Name the blood parasite species.
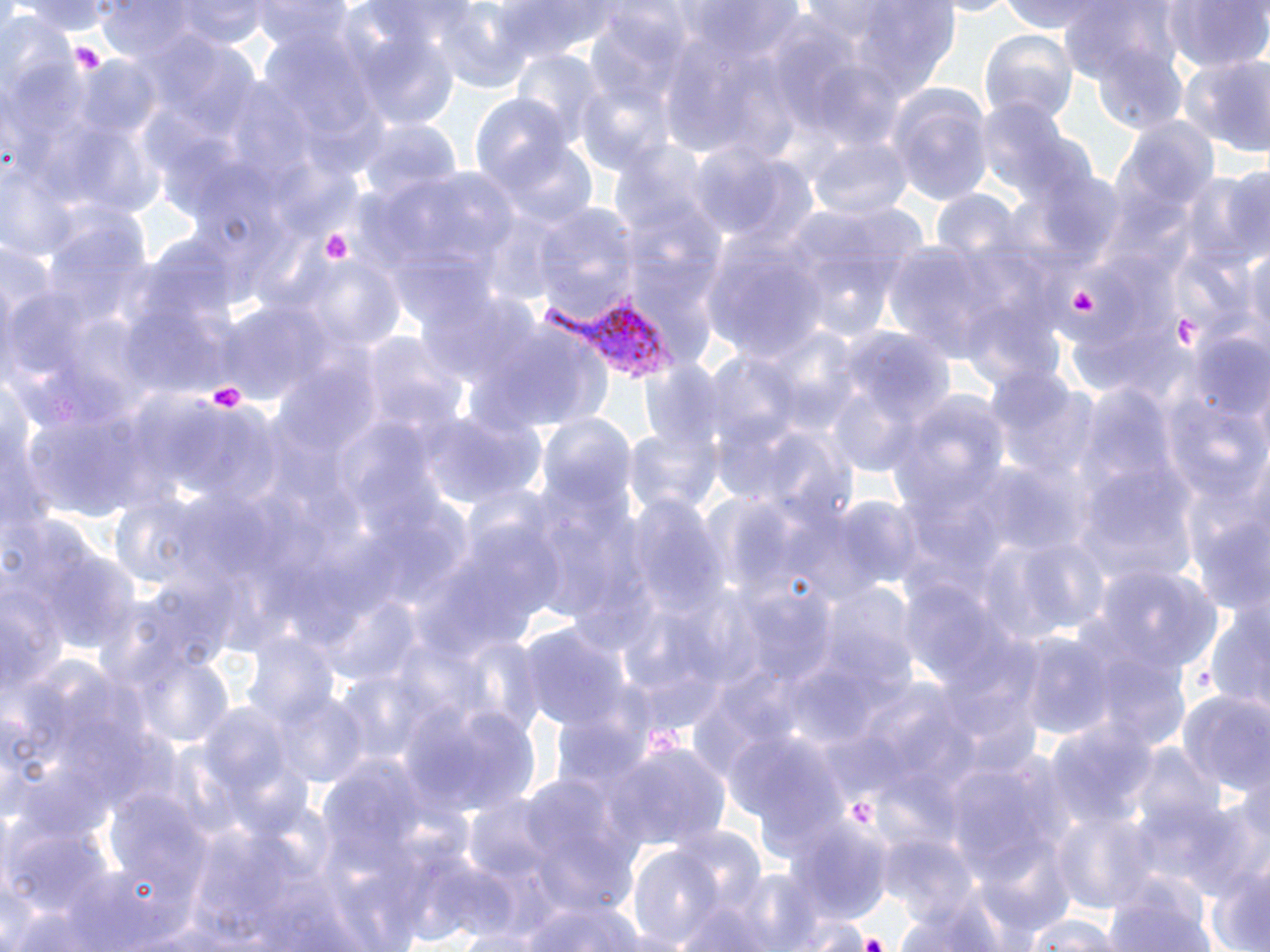
Plasmodium vivax.

Approximate bounding boxes as named x1/y1/x2/y2 corners in pixels. Plasmodium vivax-infected red blood cell locations: (x1=541, y1=294, x2=683, y2=387). Platelet locations: (x1=65, y1=41, x2=103, y2=73), (x1=319, y1=227, x2=355, y2=266), (x1=1070, y1=285, x2=1100, y2=315), (x1=1173, y1=315, x2=1200, y2=348), (x1=205, y1=380, x2=250, y2=417), (x1=850, y1=796, x2=877, y2=824), (x1=856, y1=931, x2=888, y2=950). Uninfected red blood cell locations: (x1=14, y1=0, x2=119, y2=35), (x1=251, y1=0, x2=357, y2=53), (x1=993, y1=0, x2=1128, y2=34), (x1=1161, y1=0, x2=1270, y2=76), (x1=176, y1=1, x2=270, y2=47), (x1=499, y1=1, x2=626, y2=59), (x1=831, y1=2, x2=963, y2=98), (x1=1056, y1=2, x2=1181, y2=78), (x1=98, y1=3, x2=198, y2=60), (x1=425, y1=5, x2=539, y2=91), (x1=0, y1=16, x2=81, y2=103), (x1=351, y1=22, x2=463, y2=130), (x1=978, y1=31, x2=1078, y2=122), (x1=1090, y1=41, x2=1190, y2=135), (x1=512, y1=49, x2=609, y2=147), (x1=1182, y1=53, x2=1270, y2=160), (x1=75, y1=61, x2=165, y2=146), (x1=575, y1=86, x2=675, y2=178), (x1=888, y1=86, x2=991, y2=204), (x1=469, y1=92, x2=575, y2=203), (x1=976, y1=98, x2=1077, y2=205), (x1=1119, y1=117, x2=1219, y2=219), (x1=358, y1=119, x2=461, y2=208), (x1=807, y1=136, x2=912, y2=223), (x1=496, y1=139, x2=599, y2=229), (x1=1185, y1=169, x2=1270, y2=267), (x1=930, y1=191, x2=1023, y2=272), (x1=620, y1=197, x2=727, y2=338), (x1=531, y1=206, x2=642, y2=324), (x1=701, y1=229, x2=832, y2=364), (x1=1241, y1=242, x2=1270, y2=365), (x1=289, y1=254, x2=403, y2=360), (x1=418, y1=285, x2=535, y2=386), (x1=219, y1=300, x2=336, y2=407), (x1=470, y1=317, x2=610, y2=435), (x1=357, y1=329, x2=468, y2=440), (x1=1192, y1=335, x2=1270, y2=424), (x1=1, y1=381, x2=48, y2=544), (x1=888, y1=392, x2=1010, y2=520), (x1=422, y1=411, x2=545, y2=513), (x1=624, y1=422, x2=724, y2=522), (x1=1075, y1=477, x2=1199, y2=591), (x1=618, y1=494, x2=725, y2=624), (x1=995, y1=533, x2=1111, y2=644), (x1=1094, y1=568, x2=1222, y2=673), (x1=0, y1=582, x2=61, y2=705), (x1=1203, y1=607, x2=1270, y2=712), (x1=516, y1=622, x2=635, y2=738), (x1=1008, y1=627, x2=1116, y2=739), (x1=244, y1=633, x2=342, y2=730), (x1=127, y1=647, x2=237, y2=749), (x1=1083, y1=650, x2=1191, y2=755), (x1=269, y1=691, x2=369, y2=786), (x1=1181, y1=691, x2=1270, y2=795), (x1=408, y1=699, x2=541, y2=820), (x1=198, y1=705, x2=296, y2=808), (x1=1051, y1=724, x2=1158, y2=827), (x1=604, y1=739, x2=729, y2=857), (x1=1135, y1=744, x2=1224, y2=832), (x1=939, y1=759, x2=1068, y2=893), (x1=1166, y1=796, x2=1267, y2=902), (x1=1053, y1=811, x2=1156, y2=914), (x1=788, y1=823, x2=891, y2=921), (x1=877, y1=836, x2=985, y2=931), (x1=628, y1=846, x2=725, y2=949), (x1=1205, y1=865, x2=1270, y2=952), (x1=1103, y1=884, x2=1219, y2=951), (x1=890, y1=897, x2=1011, y2=952), (x1=667, y1=898, x2=780, y2=952), (x1=512, y1=900, x2=646, y2=951), (x1=1020, y1=911, x2=1130, y2=952). Single field of view. Image is 1270×952 pixels. Optical microscopy. May-Grünwald-Giemsa-stained preparation. Thin blood film. 1000x magnification.